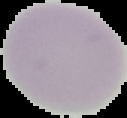

malaria status = uninfected
preparation = thin blood smear
image size = 127×118 pixels
image type = cell region segmented out of the field of view; surrounding area masked to black